Classify this cell by malaria status.
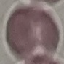
Uninfected.

image type = cell patch, automatically extracted from a larger field of view and resized to 64 × 64 pixels
preparation = thin blood smear
stain = Giemsa
capture = smartphone camera at the microscope eyepiece